State which parasite is depicted.
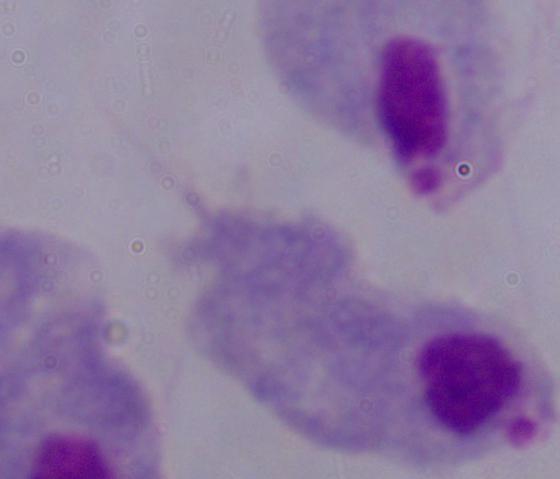
A trichomonad.

1000x magnification. Photomicrograph.